Assess this cell for malaria.
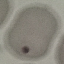

It is uninfected.

Thin blood smear. Giemsa-stained preparation. Automatically extracted cell patch, resized to 64 × 64 pixels. Acquired by smartphone through the microscope eyepiece.